Report the malaria status of this cell.
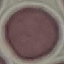
It is uninfected.

Giemsa stain. Automatically extracted cell patch, resized to 64 × 64 pixels. Acquired by smartphone through the microscope eyepiece. Thin smear of blood.